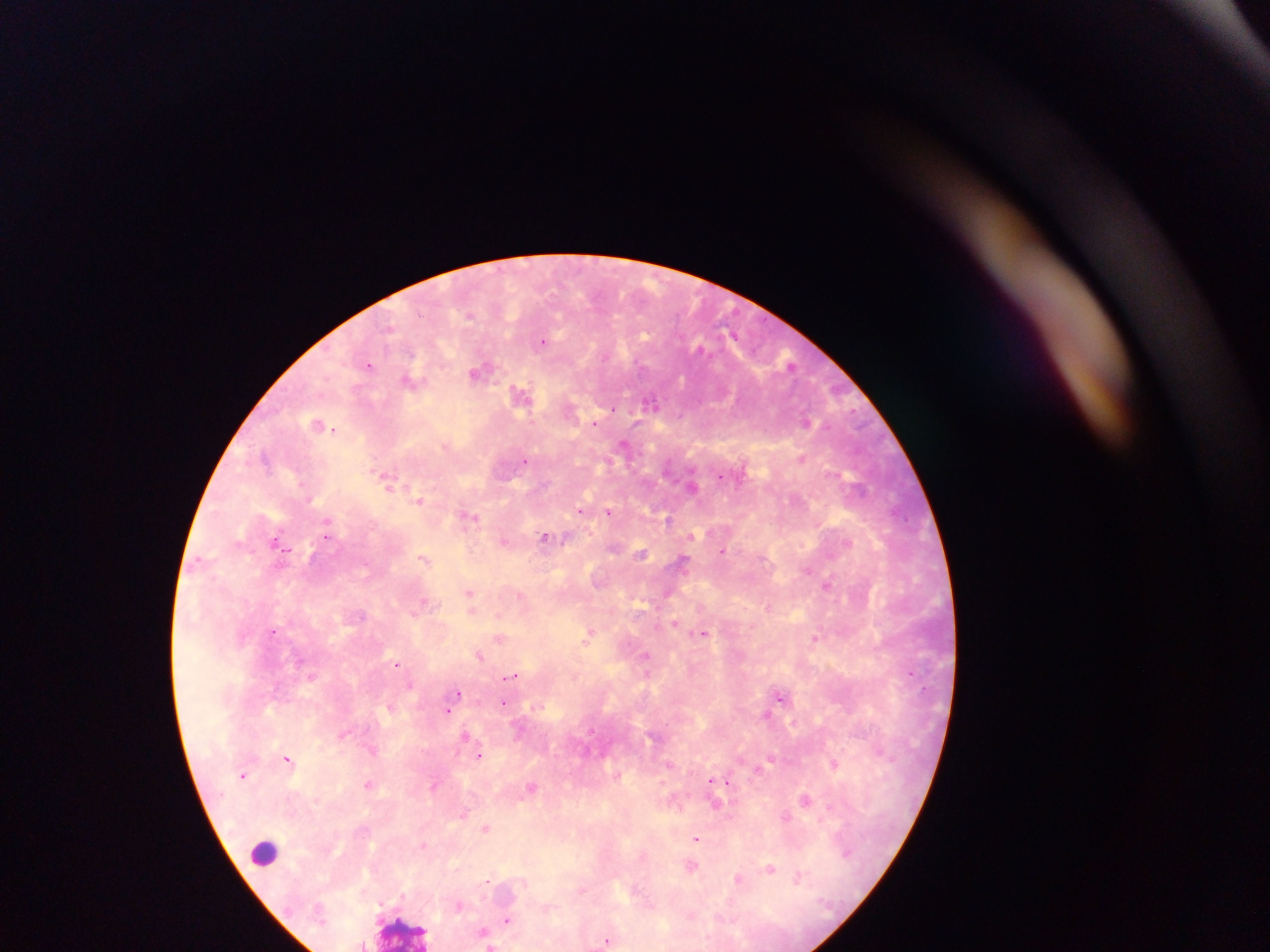

{
  "image_size": "1270×952 pixels",
  "preparation": "thick blood film",
  "plasmodium_parasite_locations": "approximate centers as {x, y} in pixels: {422, 314}, {470, 316}, {645, 334}, {543, 343}, {369, 365}, {477, 372}, {520, 392}, {651, 401}, {611, 407}, {808, 422}, {334, 430}, {624, 441}, {802, 457}, {526, 463}, {720, 476}, {849, 478}, {388, 481}, {419, 500}, {583, 509}, {609, 511}, {469, 517}, {667, 517}, {327, 522}, {545, 537}, {847, 543}, {276, 544}, {287, 550}, {725, 551}, {311, 554}, {642, 554}, {424, 559}, {684, 561}, {828, 582}, {469, 591}, {521, 596}, {423, 600}, {471, 609}, {498, 613}, {363, 615}, {676, 622}, {274, 630}, {705, 632}, {589, 636}, {816, 636}, {500, 637}, {644, 653}, {480, 655}, {397, 662}, {909, 672}, {511, 676}, {458, 692}, {783, 697}, {503, 703}, {448, 710}, {465, 734}, {344, 735}, {480, 754}, {287, 758}, {772, 760}, {834, 765}, {243, 775}, {722, 780}, {712, 781}, {369, 783}, {432, 786}, {531, 786}, {808, 798}, {829, 805}, {462, 813}, {786, 815}, {486, 829}, {696, 837}, {423, 846}, {692, 867}, {771, 867}, {800, 875}, {738, 879}, {525, 883}, {582, 892}, {458, 905}, {690, 915}, {506, 918}, {482, 931}, {606, 941}, {491, 944}",
  "field_of_view": "single",
  "capture": "mobile-phone photograph through a microscope",
  "country": "Ghana",
  "leukocyte_locations": "approximate centers as {x, y} in pixels: {267, 857}, {400, 932}"
}